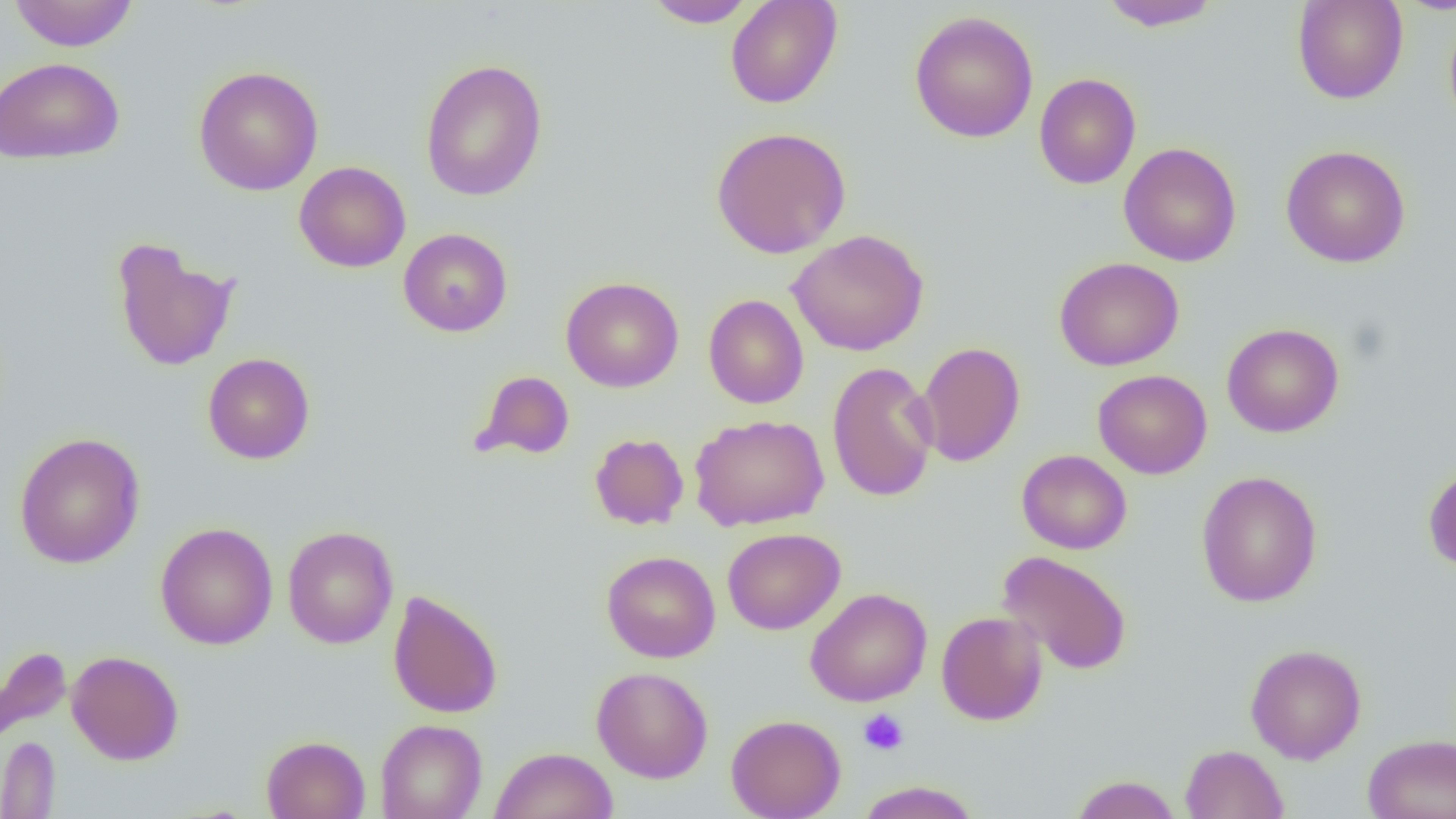

{
  "slide_level_diagnosis": "negative for blood parasites",
  "platelet_locations": "approximate bounding boxes as (x1,y1)-(x2,y2) corner pairs in pixels: (858,709)-(909,755)",
  "modality": "light microscopy",
  "image_size": "1456×819 pixels",
  "field_of_view": "single",
  "preparation": "thin blood film",
  "magnification": "1000x",
  "uninfected_red_blood_cell_locations": "approximate bounding boxes as (x1,y1)-(x2,y2) corner pairs in pixels: (8,0)-(139,51), (642,0)-(758,28), (725,0)-(842,109), (1099,0)-(1220,31), (1292,0)-(1409,104), (910,10)-(1039,143), (1444,10)-(1456,134), (0,56)-(124,164), (420,59)-(549,201), (193,65)-(324,196), (1034,73)-(1141,189), (711,126)-(851,258), (1118,142)-(1241,267), (1281,144)-(1410,267), (294,161)-(411,273), (398,227)-(513,337), (787,230)-(929,356), (110,238)-(240,372), (1054,256)-(1184,372), (560,276)-(684,393), (703,294)-(809,409), (1221,323)-(1344,438), (915,341)-(1025,467), (202,352)-(315,464), (826,361)-(939,503), (1093,369)-(1212,479), (471,370)-(576,462), (689,414)-(829,531), (14,432)-(145,569), (589,433)-(689,530), (1016,449)-(1132,554), (1423,464)-(1456,571), (1195,470)-(1323,607), (155,522)-(278,649), (283,525)-(399,649), (722,527)-(845,635), (601,550)-(720,663), (997,550)-(1133,676), (805,587)-(932,707), (387,589)-(503,719), (936,610)-(1048,725), (1245,644)-(1367,764), (0,645)-(72,744), (66,650)-(184,765), (591,666)-(713,783), (726,714)-(846,819), (375,718)-(487,819), (1362,734)-(1456,819), (0,735)-(61,818), (261,735)-(370,819), (1180,744)-(1289,819), (490,746)-(617,819), (1069,775)-(1183,819), (855,781)-(982,819)"
}